Identify the parasite.
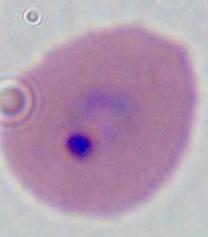

This is Plasmodium.

Micrograph. Captured at either 400x or 1000x magnification.